Describe the morphology of the erythrocytes.
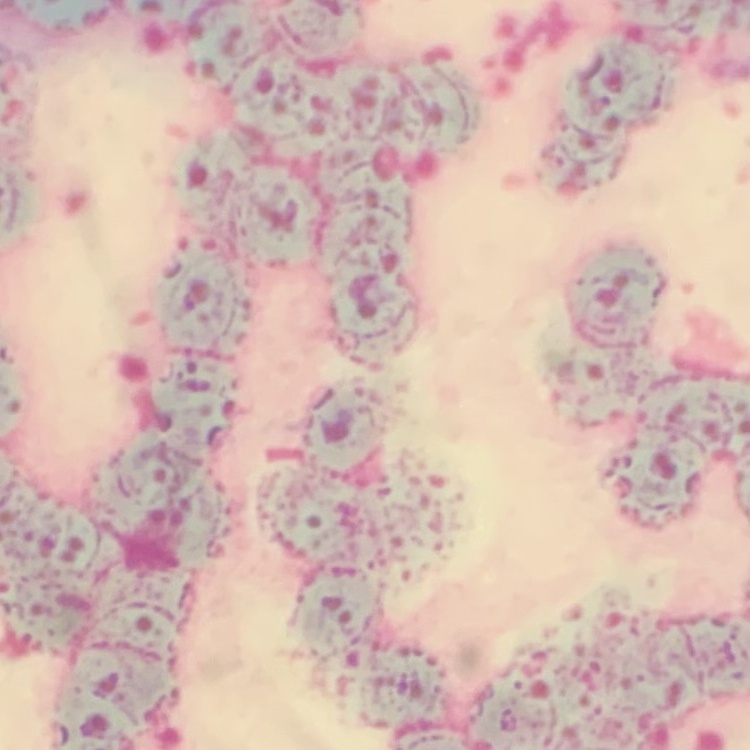

Rouleaux formation.

image type = square crop of a larger photomicrograph
stain = Field's or Giemsa
preparation = thin blood film